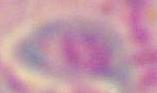
Summary:
  - Identification: Toxoplasma gondii
  - Magnification: 1000x
  - Modality: micrograph